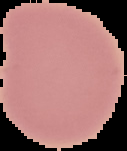

image_type: cell region segmented out of the field of view; surrounding area masked to black
result: negative for malaria parasites
image_size: 127×151 pixels
preparation: thin blood film